Name the parasite shown.
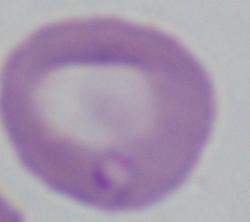
This is Babesia.

modality = micrograph
magnification = 1000x